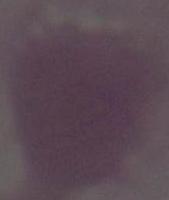

Photomicrograph. An erythrocyte is shown. 1000x magnification.